Assess the morphology of the red blood cells.
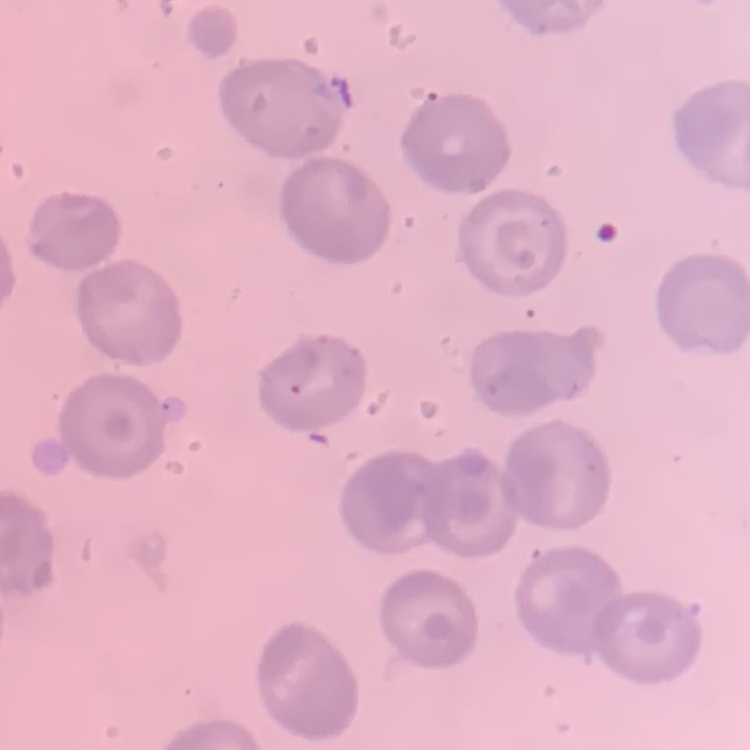

No rouleaux formation.

{
  "stain": "Field's or Giemsa",
  "image_type": "one tile cut from a larger photomicrograph",
  "preparation": "thin peripheral smear"
}